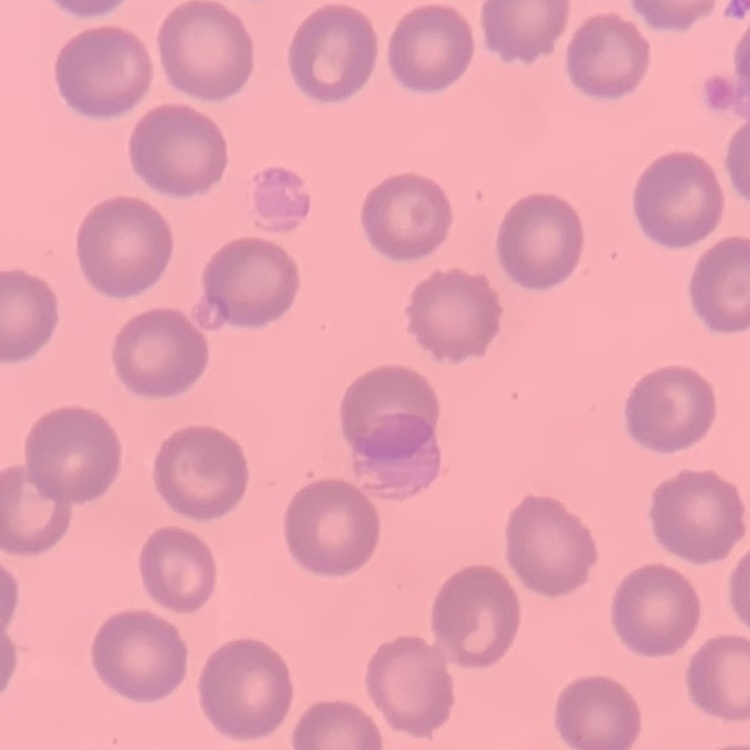
The erythrocytes show no rouleaux formation. Thin blood film. Stained with either Field's or Giemsa. One tile cut from a larger photomicrograph.